Locate every blood parasite and identify its species.
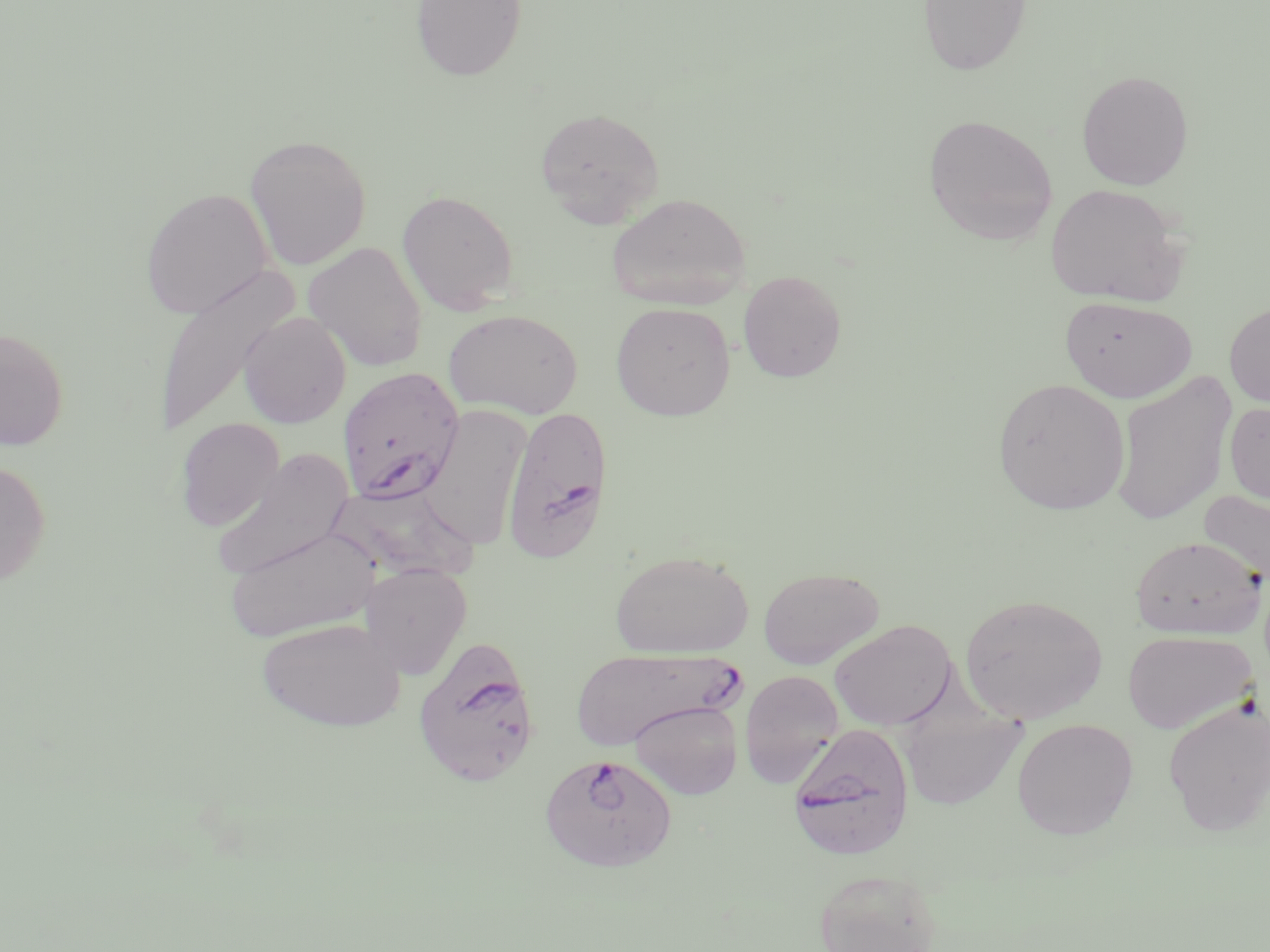

Approximate bounding boxes as named x1/y1/x2/y2 corners in pixels.
Plasmodium falciparum-infected red blood cells: (x1=337, y1=367, x2=464, y2=503), (x1=500, y1=404, x2=614, y2=564), (x1=412, y1=636, x2=541, y2=788), (x1=570, y1=648, x2=735, y2=748), (x1=788, y1=723, x2=915, y2=861), (x1=546, y1=751, x2=679, y2=874).
No Plasmodium ovale, Plasmodium malariae, Plasmodium vivax, Babesia divergens, or Trypanosoma brucei observed.

Uninfected red blood cell locations: (x1=411, y1=0, x2=526, y2=81), (x1=919, y1=0, x2=1032, y2=76), (x1=1076, y1=70, x2=1194, y2=191), (x1=534, y1=106, x2=665, y2=226), (x1=923, y1=114, x2=1058, y2=246), (x1=244, y1=133, x2=372, y2=271), (x1=1045, y1=183, x2=1187, y2=306), (x1=140, y1=187, x2=275, y2=319), (x1=396, y1=189, x2=519, y2=314), (x1=606, y1=193, x2=751, y2=309), (x1=303, y1=241, x2=428, y2=371), (x1=150, y1=265, x2=299, y2=439), (x1=737, y1=270, x2=847, y2=382), (x1=1060, y1=295, x2=1198, y2=403), (x1=610, y1=301, x2=736, y2=421), (x1=1223, y1=301, x2=1270, y2=408), (x1=444, y1=308, x2=583, y2=419), (x1=239, y1=311, x2=352, y2=428), (x1=0, y1=328, x2=69, y2=450), (x1=1110, y1=371, x2=1236, y2=527), (x1=992, y1=377, x2=1130, y2=515), (x1=1224, y1=403, x2=1270, y2=505), (x1=422, y1=404, x2=531, y2=552), (x1=174, y1=418, x2=284, y2=532), (x1=211, y1=449, x2=354, y2=581), (x1=0, y1=461, x2=51, y2=586), (x1=325, y1=481, x2=482, y2=584), (x1=1198, y1=487, x2=1270, y2=594), (x1=224, y1=526, x2=380, y2=642), (x1=1130, y1=536, x2=1266, y2=640), (x1=610, y1=549, x2=755, y2=659), (x1=358, y1=564, x2=471, y2=679), (x1=758, y1=566, x2=884, y2=669), (x1=959, y1=593, x2=1108, y2=724), (x1=255, y1=617, x2=406, y2=732), (x1=829, y1=619, x2=957, y2=730), (x1=1122, y1=629, x2=1258, y2=734), (x1=738, y1=670, x2=844, y2=789), (x1=1162, y1=697, x2=1270, y2=836), (x1=629, y1=700, x2=743, y2=800), (x1=898, y1=710, x2=1028, y2=810), (x1=1011, y1=718, x2=1138, y2=840), (x1=812, y1=867, x2=945, y2=952). Slide-level diagnosis: Plasmodium falciparum. May-Grünwald-Giemsa stain. Light microscopy. Single field of view. Image is 1270×952 pixels. Captured at 1000x magnification. Thin blood smear.